Name the blood parasite species.
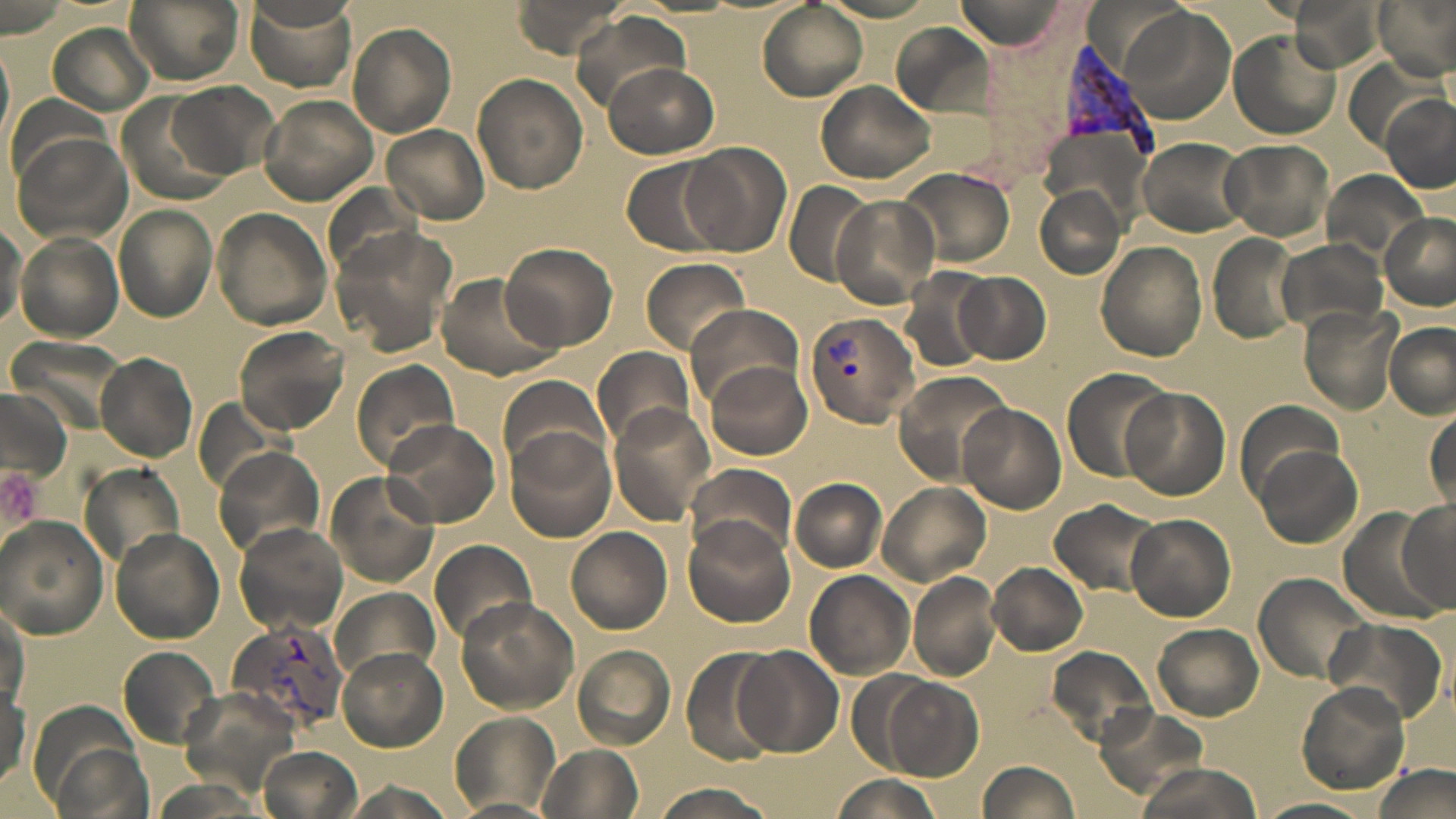
Plasmodium vivax.

preparation = thin blood film
field of view = one of a larger specimen
uninfected red blood cell locations = approximate bounding boxes as named x1/y1/x2/y2 corners in pixels: (x1=125, y1=0, x2=244, y2=83), (x1=509, y1=0, x2=628, y2=58), (x1=952, y1=0, x2=1073, y2=50), (x1=1374, y1=0, x2=1456, y2=78), (x1=242, y1=1, x2=356, y2=92), (x1=757, y1=2, x2=866, y2=102), (x1=1118, y1=6, x2=1238, y2=120), (x1=573, y1=14, x2=689, y2=111), (x1=347, y1=24, x2=457, y2=137), (x1=51, y1=25, x2=152, y2=114), (x1=1228, y1=30, x2=1341, y2=139), (x1=1348, y1=58, x2=1438, y2=151), (x1=602, y1=61, x2=720, y2=159), (x1=473, y1=73, x2=588, y2=193), (x1=816, y1=80, x2=936, y2=184), (x1=172, y1=82, x2=278, y2=178), (x1=1380, y1=95, x2=1456, y2=192), (x1=259, y1=96, x2=378, y2=204), (x1=384, y1=125, x2=489, y2=224), (x1=1136, y1=137, x2=1250, y2=236), (x1=1221, y1=138, x2=1335, y2=242), (x1=680, y1=142, x2=792, y2=257), (x1=619, y1=155, x2=733, y2=258), (x1=900, y1=167, x2=1015, y2=265), (x1=1324, y1=171, x2=1426, y2=258), (x1=783, y1=182, x2=877, y2=286), (x1=1033, y1=185, x2=1128, y2=280), (x1=829, y1=194, x2=941, y2=308), (x1=114, y1=204, x2=219, y2=324), (x1=212, y1=208, x2=332, y2=331), (x1=1382, y1=214, x2=1455, y2=311), (x1=0, y1=218, x2=28, y2=333), (x1=328, y1=226, x2=456, y2=357), (x1=13, y1=232, x2=124, y2=343), (x1=1209, y1=234, x2=1300, y2=342), (x1=1279, y1=240, x2=1388, y2=336), (x1=1096, y1=241, x2=1208, y2=361), (x1=501, y1=243, x2=616, y2=351), (x1=638, y1=257, x2=752, y2=356), (x1=900, y1=270, x2=995, y2=373), (x1=434, y1=271, x2=562, y2=381), (x1=956, y1=271, x2=1051, y2=365), (x1=685, y1=302, x2=801, y2=409), (x1=1299, y1=307, x2=1402, y2=414), (x1=1381, y1=321, x2=1456, y2=416), (x1=234, y1=325, x2=350, y2=434), (x1=591, y1=346, x2=694, y2=448), (x1=95, y1=350, x2=201, y2=463), (x1=351, y1=360, x2=459, y2=471), (x1=707, y1=363, x2=812, y2=459), (x1=1064, y1=368, x2=1177, y2=485), (x1=895, y1=371, x2=1015, y2=482), (x1=497, y1=373, x2=611, y2=478), (x1=1120, y1=388, x2=1231, y2=501), (x1=957, y1=404, x2=1066, y2=513), (x1=609, y1=406, x2=717, y2=523), (x1=1425, y1=408, x2=1455, y2=513), (x1=382, y1=417, x2=501, y2=528), (x1=505, y1=426, x2=616, y2=543), (x1=1255, y1=445, x2=1363, y2=547), (x1=215, y1=449, x2=322, y2=553), (x1=686, y1=461, x2=797, y2=563), (x1=327, y1=471, x2=439, y2=588), (x1=791, y1=479, x2=887, y2=571), (x1=879, y1=483, x2=989, y2=585), (x1=1050, y1=498, x2=1163, y2=597), (x1=1395, y1=498, x2=1455, y2=613), (x1=1339, y1=510, x2=1447, y2=622), (x1=1124, y1=513, x2=1235, y2=621), (x1=0, y1=515, x2=107, y2=640), (x1=683, y1=517, x2=795, y2=627), (x1=233, y1=522, x2=349, y2=636), (x1=566, y1=526, x2=673, y2=634), (x1=112, y1=529, x2=224, y2=643), (x1=430, y1=538, x2=537, y2=648), (x1=988, y1=563, x2=1087, y2=655), (x1=806, y1=572, x2=915, y2=680), (x1=908, y1=572, x2=998, y2=681), (x1=1253, y1=572, x2=1372, y2=685), (x1=330, y1=586, x2=440, y2=691), (x1=455, y1=597, x2=579, y2=715), (x1=1, y1=599, x2=29, y2=712), (x1=1328, y1=616, x2=1448, y2=725), (x1=1153, y1=624, x2=1263, y2=720), (x1=118, y1=644, x2=221, y2=750), (x1=572, y1=644, x2=675, y2=750), (x1=737, y1=645, x2=844, y2=758), (x1=1045, y1=645, x2=1157, y2=752), (x1=338, y1=648, x2=447, y2=752), (x1=680, y1=648, x2=784, y2=764), (x1=881, y1=675, x2=984, y2=782), (x1=0, y1=682, x2=28, y2=791), (x1=1296, y1=683, x2=1409, y2=795), (x1=1096, y1=705, x2=1211, y2=799), (x1=451, y1=711, x2=559, y2=812), (x1=261, y1=745, x2=361, y2=819), (x1=541, y1=746, x2=643, y2=819), (x1=1133, y1=760, x2=1266, y2=819), (x1=978, y1=761, x2=1081, y2=818), (x1=1372, y1=763, x2=1454, y2=817), (x1=828, y1=776, x2=945, y2=819), (x1=340, y1=779, x2=459, y2=819), (x1=650, y1=784, x2=779, y2=819), (x1=1259, y1=795, x2=1377, y2=819)
image size = 1456×819 pixels
Plasmodium vivax-infected red blood cell locations = approximate bounding boxes as named x1/y1/x2/y2 corners in pixels: (x1=1062, y1=42, x2=1156, y2=159), (x1=804, y1=314, x2=916, y2=427), (x1=227, y1=618, x2=350, y2=738)
stain = May-Grünwald-Giemsa
modality = optical microscopy
magnification = 1000x